Outline each blood parasite and name the species.
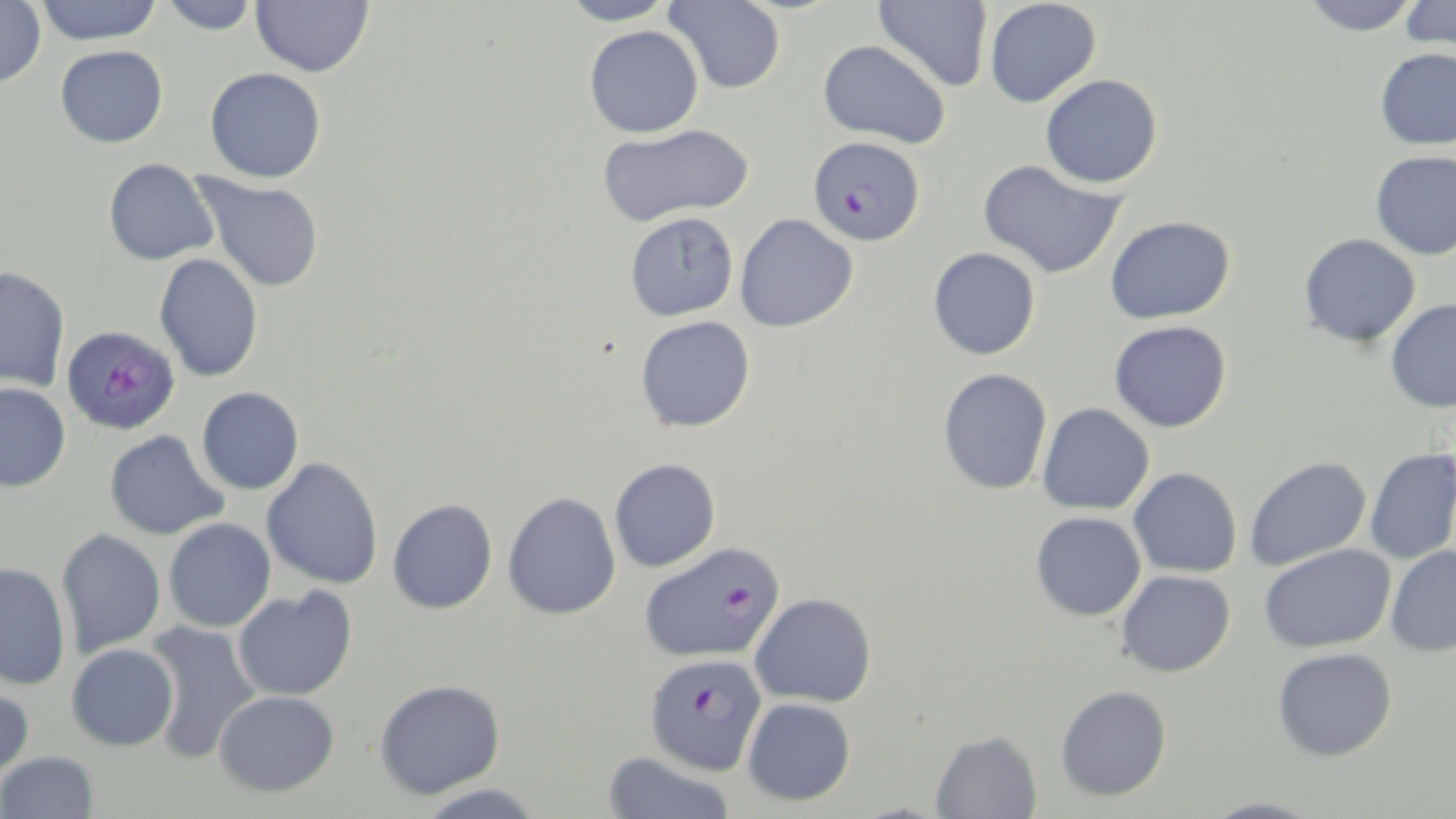

Approximate bounding boxes as (x1,y1)-(x2,y2) corner pairs in pixels.
Plasmodium falciparum-infected red blood cells: (808,135)-(925,246), (61,324)-(180,435), (639,541)-(785,663), (644,653)-(768,776).
No Plasmodium ovale, Plasmodium malariae, Plasmodium vivax, Babesia divergens, or Trypanosoma brucei observed.

slide-level diagnosis = Plasmodium falciparum
magnification = 1000x
field of view = single
stain = May-Grünwald-Giemsa
uninfected red blood cell locations = approximate bounding boxes as (x1,y1)-(x2,y2) corner pairs in pixels: (34,0)-(164,45), (158,0)-(260,35), (251,0)-(374,77), (561,0)-(676,27), (665,0)-(786,94), (873,0)-(993,92), (1301,0)-(1421,36), (1399,0)-(1456,54), (0,1)-(46,88), (984,1)-(1102,108), (584,25)-(704,138), (818,39)-(950,148), (56,45)-(168,148), (1375,47)-(1456,151), (204,68)-(326,183), (1040,74)-(1163,189), (597,123)-(754,226), (1370,150)-(1456,261), (104,158)-(218,265), (978,159)-(1126,279), (193,173)-(324,293), (625,212)-(739,321), (735,213)-(858,332), (1105,215)-(1236,324), (1299,233)-(1420,347), (928,247)-(1041,360), (154,253)-(263,382), (0,266)-(70,392), (1385,299)-(1456,413), (635,315)-(755,432), (1109,320)-(1231,432), (938,368)-(1053,495), (0,382)-(71,492), (196,387)-(304,494), (1037,402)-(1155,515), (105,429)-(229,541), (1365,448)-(1456,564), (1245,456)-(1371,569), (261,458)-(384,590), (609,458)-(721,572), (1128,467)-(1242,578), (503,491)-(621,620), (387,498)-(498,614), (1031,511)-(1146,621), (163,518)-(276,633), (56,529)-(166,657), (1259,543)-(1395,653), (1385,545)-(1456,657), (0,562)-(72,691), (1117,570)-(1236,677), (233,586)-(357,701), (749,593)-(876,708), (142,621)-(262,763), (66,643)-(179,751), (1272,646)-(1397,761), (375,678)-(505,799), (0,680)-(34,781), (1056,684)-(1172,801), (214,690)-(340,796), (742,697)-(856,806), (930,729)-(1042,819), (1,751)-(99,818), (601,752)-(736,819), (414,784)-(546,818), (1197,798)-(1326,819)
image size = 1456×819 pixels
preparation = thin blood film
modality = light microscopy